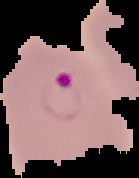

Summary:
  - Result: malaria parasites detected
  - Preparation: thin blood smear
  - Image type: segmented cell region on a black background
  - Image size: 139×178 pixels